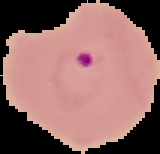

Summary:
  - Image type: cell region segmented out of the field of view; surrounding area masked to black
  - Preparation: thin blood smear
  - Image size: 160×154 pixels
  - Result: Plasmodium parasites identified